State which cell type is depicted.
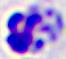
A leukocyte.

Micrograph. Captured at 400x magnification.